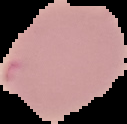 Image is 127×124 pixels. The area outside the segmented cell region is set to black. Malaria status: parasitized. From a thin blood film.